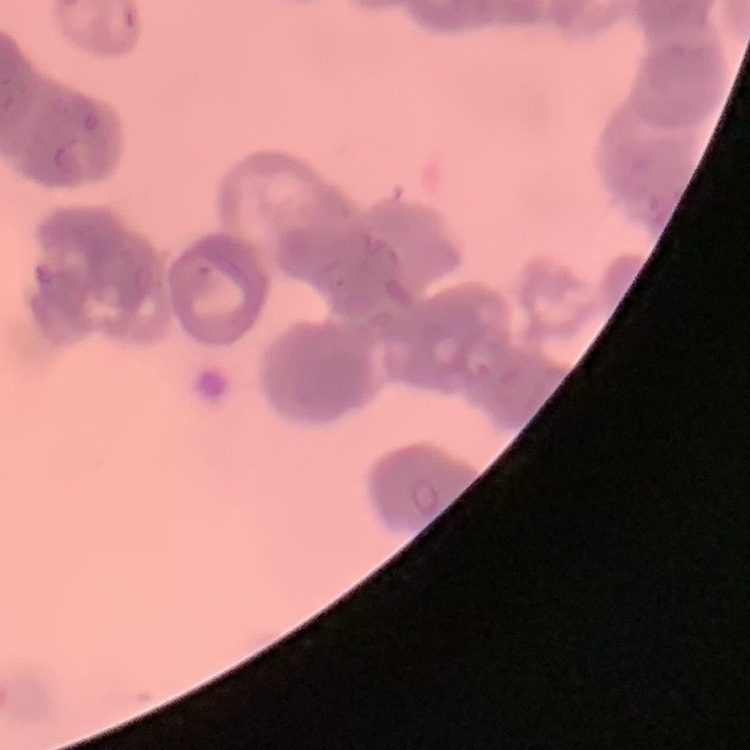
red blood cell morphology = rouleaux formation
image type = square crop of a larger photomicrograph
preparation = thin peripheral smear
stain = Field's or Giemsa